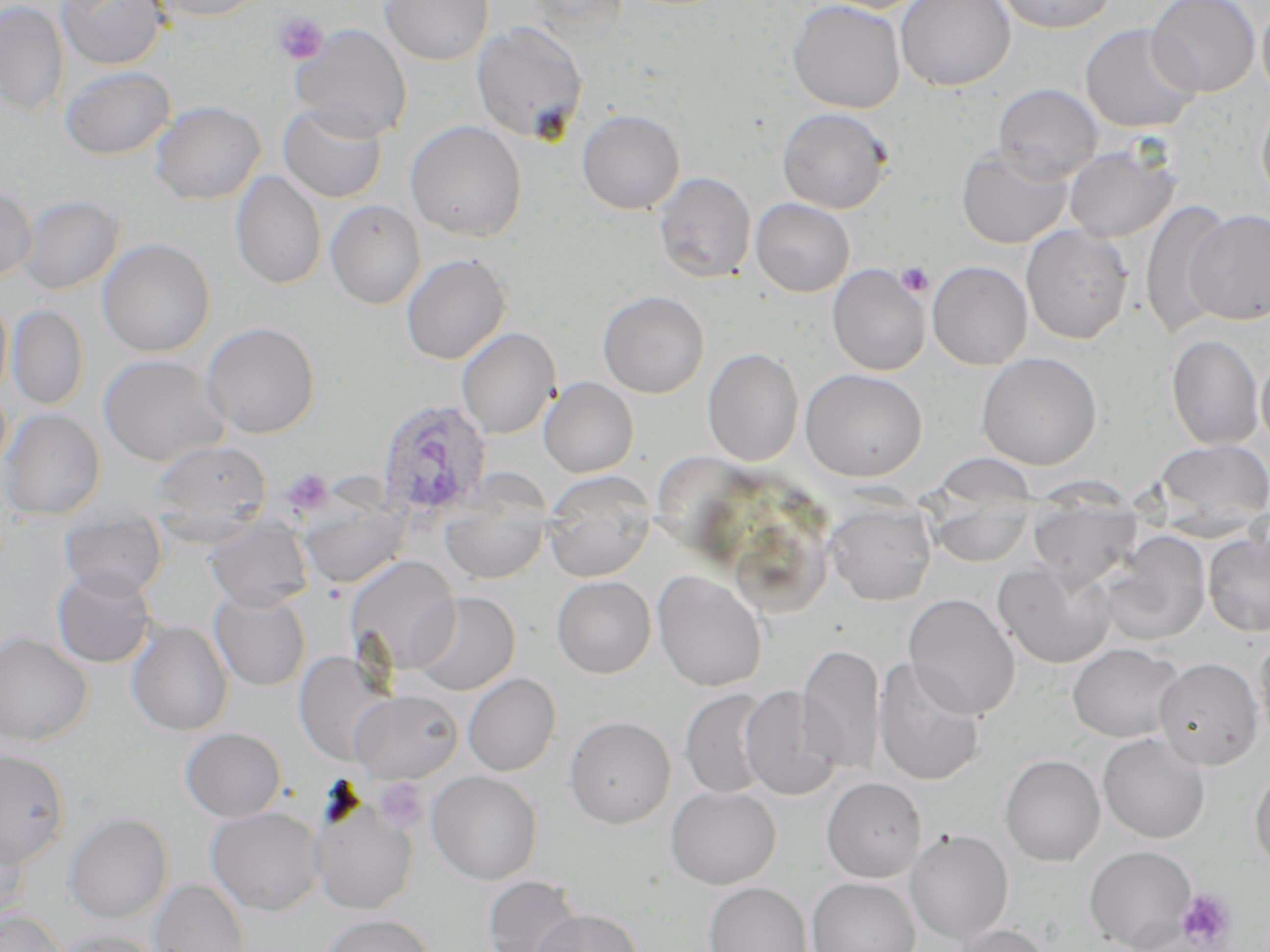 Approximate bounding boxes as (x1,y1)-(x2,y2) corner pairs in pixels. Platelet locations: (274,13)-(329,65), (896,262)-(934,298), (282,469)-(334,516), (375,777)-(429,832), (1176,889)-(1236,949). Plasmodium ovale-infected red blood cell locations: (374,398)-(493,520). Uninfected red blood cell locations: (57,0)-(169,71), (149,0)-(270,21), (380,0)-(493,65), (525,0)-(634,43), (788,0)-(905,113), (815,0)-(935,13), (895,0)-(1015,91), (994,0)-(1118,33), (1147,0)-(1261,98), (0,1)-(69,117), (1257,4)-(1270,105), (471,21)-(589,144), (1081,23)-(1201,133), (290,24)-(412,142), (60,65)-(176,160), (993,83)-(1103,182), (1257,98)-(1270,208), (150,100)-(266,205), (278,102)-(388,203), (777,107)-(893,213), (577,109)-(684,215), (406,120)-(527,241), (1064,143)-(1179,243), (956,146)-(1072,249), (231,171)-(327,289), (653,171)-(756,283), (0,186)-(37,284), (17,195)-(123,294), (751,198)-(854,296), (1140,199)-(1232,340), (325,200)-(426,309), (1186,209)-(1270,325), (1021,225)-(1133,344), (97,238)-(216,357), (401,253)-(511,364), (928,261)-(1032,369), (827,263)-(931,376), (597,290)-(709,398), (0,295)-(12,399), (8,305)-(88,409), (202,322)-(320,438), (456,327)-(560,439), (1167,334)-(1264,449), (703,348)-(804,466), (976,352)-(1102,470), (98,353)-(230,467), (1256,353)-(1270,451), (800,369)-(928,481), (539,377)-(639,477), (1,409)-(105,521), (1153,439)-(1270,531), (148,440)-(271,540), (931,453)-(1040,509), (543,473)-(656,581), (928,492)-(1034,567), (440,493)-(551,584), (1027,496)-(1143,589), (301,500)-(410,589), (825,500)-(937,605), (60,513)-(167,600), (206,518)-(313,610), (1101,532)-(1211,645), (1203,533)-(1270,636), (346,556)-(461,674), (993,562)-(1117,669), (52,566)-(157,669), (652,570)-(767,692), (552,575)-(656,678), (210,588)-(311,690), (411,591)-(520,696), (903,593)-(1020,720), (127,620)-(233,735), (0,632)-(93,745), (1254,633)-(1270,749), (1067,642)-(1185,743), (797,643)-(885,775), (293,651)-(392,764), (873,657)-(985,786), (1154,657)-(1264,770), (463,673)-(560,776), (739,686)-(845,800), (680,689)-(777,798), (350,690)-(463,783), (564,715)-(676,828), (181,727)-(286,821), (1098,732)-(1210,843), (0,750)-(70,866), (1000,754)-(1105,866), (1249,765)-(1270,873), (427,771)-(543,884), (821,777)-(925,882), (666,786)-(781,889), (310,799)-(419,914), (800,804)-(934,948), (206,807)-(325,915), (64,813)-(172,923), (0,820)-(30,923), (905,829)-(1013,945), (1084,845)-(1197,951), (482,875)-(583,952), (807,877)-(920,952), (149,878)-(252,952), (704,882)-(812,952), (0,908)-(66,952), (530,909)-(644,952), (320,913)-(433,952), (947,923)-(1052,952), (51,929)-(165,952). Slide-level diagnosis: Plasmodium ovale. Image is 1270×952 pixels. May-Grünwald-Giemsa stain. 1000x magnification. Single field of view. Light microscopy. Thin blood smear.